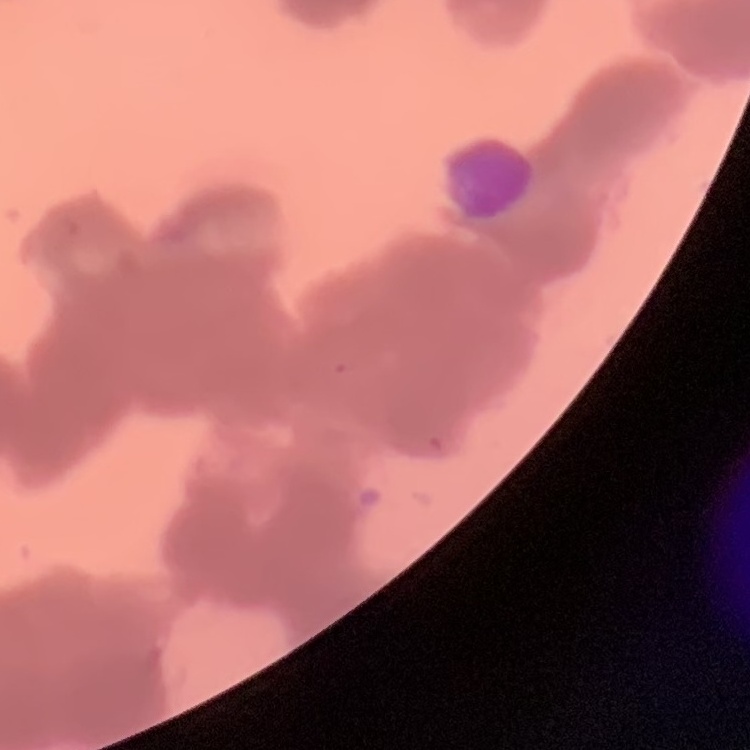

Summary:
  - Red blood cell morphology: rouleaux formation
  - Image type: square crop of a larger photomicrograph
  - Stain: Field's or Giemsa
  - Preparation: thin peripheral smear